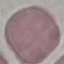

Summary:
  - Malaria status: uninfected
  - Image type: cell patch, automatically extracted from a larger field of view and resized to 64 × 64 pixels
  - Capture: smartphone through the microscope eyepiece
  - Stain: Giemsa
  - Preparation: thin blood smear